Assess this cell for malaria.
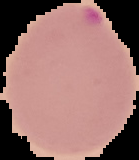

Parasitized.

Summary:
  - Preparation: thin blood smear
  - Image type: segmented cell region on a black background
  - Image size: 139×160 pixels